Give the extent of all uninfected red blood cells.
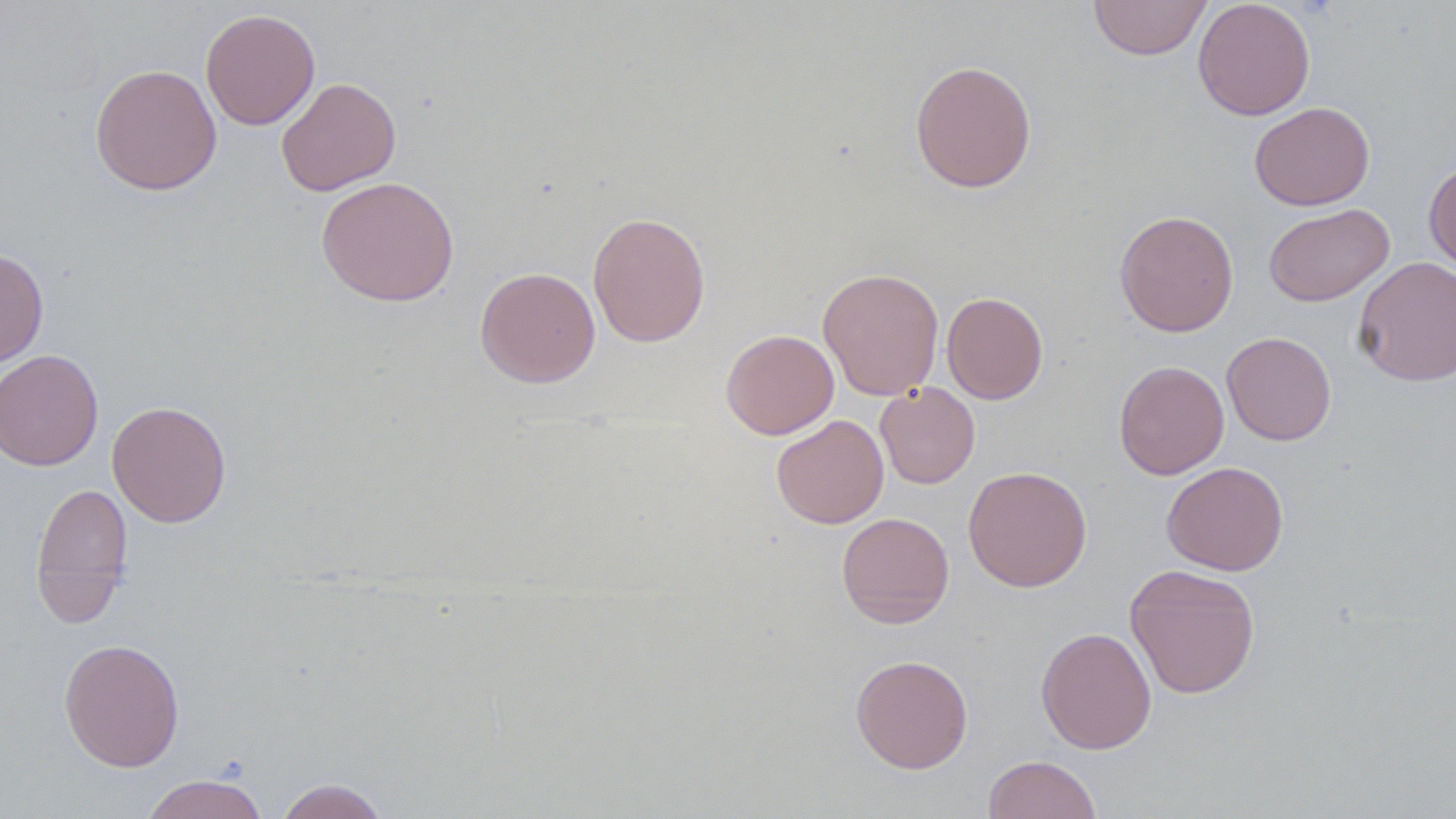

Approximate bounding boxes as (x1, y1, x2, y2) in pixels.
Uninfected red blood cells: (1193, 0, 1316, 121), (1088, 1, 1212, 60), (200, 8, 321, 131), (909, 60, 1037, 193), (90, 63, 222, 195), (276, 77, 401, 196), (1249, 102, 1375, 211), (1424, 159, 1456, 274), (316, 175, 459, 306), (1263, 203, 1394, 307), (1114, 210, 1239, 337), (588, 211, 710, 348), (0, 248, 48, 370), (1352, 256, 1456, 386), (475, 266, 600, 388), (818, 267, 944, 401), (942, 291, 1048, 404), (720, 329, 839, 439), (1221, 331, 1336, 445), (0, 349, 104, 472), (1113, 360, 1230, 480), (875, 382, 980, 488), (107, 400, 232, 528), (771, 415, 889, 529), (1162, 461, 1289, 576), (962, 465, 1093, 592), (30, 481, 133, 627), (836, 511, 954, 628), (1124, 563, 1260, 699), (1036, 626, 1157, 754), (58, 638, 185, 771), (850, 654, 973, 774), (983, 754, 1102, 818), (140, 773, 269, 819), (273, 778, 390, 819).

{
  "slide_level_diagnosis": "negative for blood parasites",
  "image_size": "1456×819 pixels",
  "magnification": "1000x",
  "field_of_view": "one of a larger specimen",
  "preparation": "thin blood film",
  "stain": "May-Grünwald-Giemsa",
  "modality": "optical microscopy"
}